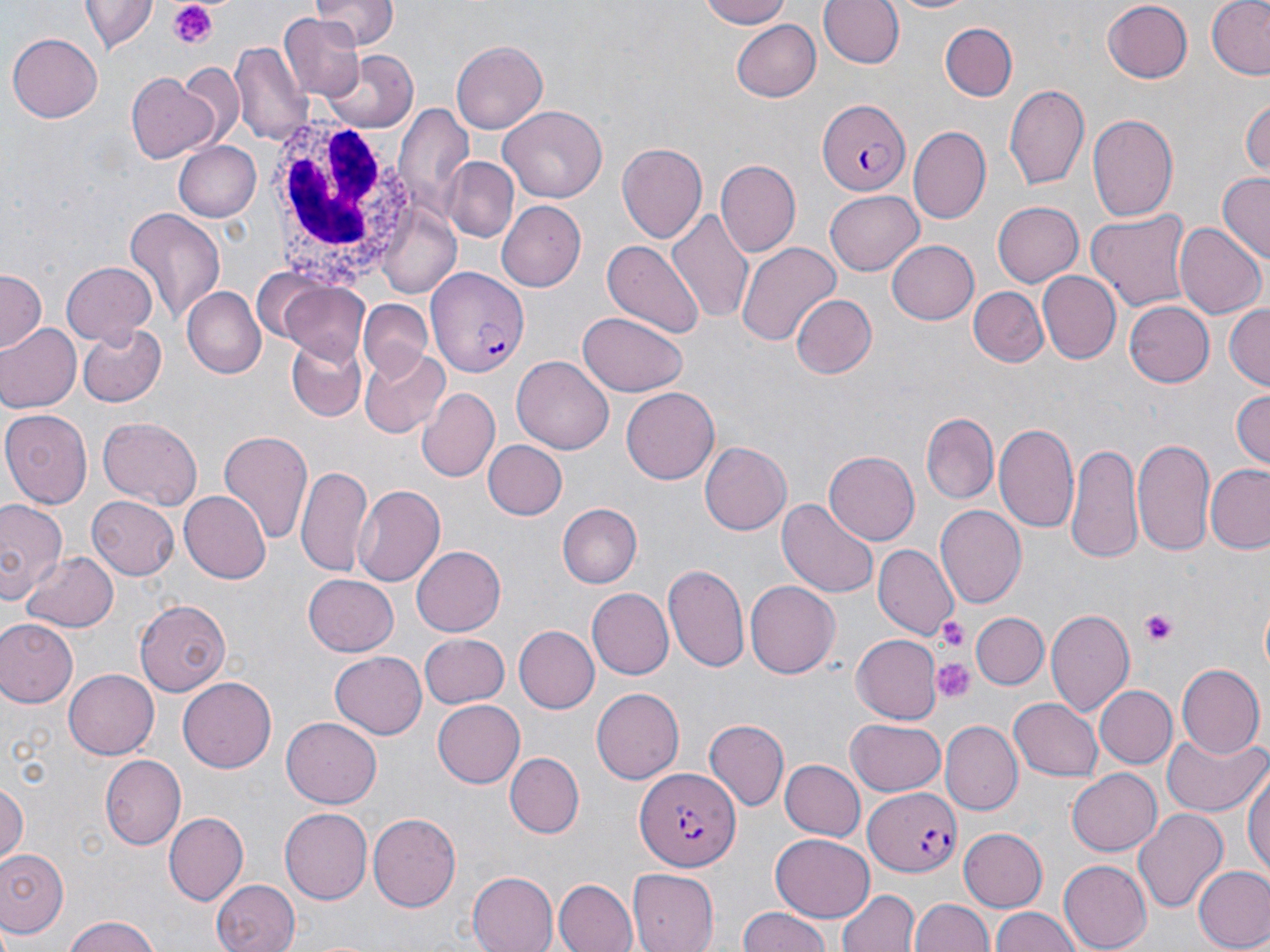 Approximate bounding boxes as named x1/y1/x2/y2 corners in pixels. White blood cell locations: (x1=257, y1=110, x2=423, y2=291). Uninfected red blood cell locations: (x1=313, y1=0, x2=396, y2=49), (x1=696, y1=0, x2=793, y2=29), (x1=819, y1=0, x2=905, y2=69), (x1=882, y1=0, x2=981, y2=16), (x1=1206, y1=0, x2=1270, y2=81), (x1=1101, y1=1, x2=1195, y2=84), (x1=82, y1=2, x2=156, y2=54), (x1=278, y1=15, x2=369, y2=101), (x1=732, y1=20, x2=821, y2=102), (x1=938, y1=20, x2=1017, y2=101), (x1=8, y1=29, x2=103, y2=120), (x1=450, y1=41, x2=546, y2=134), (x1=230, y1=42, x2=309, y2=146), (x1=324, y1=50, x2=417, y2=133), (x1=182, y1=63, x2=244, y2=145), (x1=126, y1=73, x2=220, y2=164), (x1=1005, y1=82, x2=1092, y2=191), (x1=1242, y1=97, x2=1269, y2=181), (x1=394, y1=103, x2=476, y2=220), (x1=499, y1=105, x2=609, y2=204), (x1=1088, y1=111, x2=1180, y2=226), (x1=909, y1=128, x2=990, y2=224), (x1=172, y1=139, x2=262, y2=221), (x1=615, y1=141, x2=708, y2=243), (x1=443, y1=157, x2=517, y2=239), (x1=716, y1=160, x2=800, y2=258), (x1=1217, y1=172, x2=1269, y2=265), (x1=824, y1=191, x2=924, y2=274), (x1=499, y1=200, x2=590, y2=292), (x1=993, y1=200, x2=1085, y2=287), (x1=378, y1=206, x2=461, y2=300), (x1=123, y1=208, x2=224, y2=322), (x1=668, y1=208, x2=755, y2=327), (x1=1087, y1=208, x2=1194, y2=312), (x1=1173, y1=222, x2=1265, y2=319), (x1=885, y1=240, x2=977, y2=324), (x1=602, y1=241, x2=704, y2=340), (x1=735, y1=243, x2=840, y2=350), (x1=60, y1=261, x2=157, y2=348), (x1=0, y1=271, x2=44, y2=356), (x1=1038, y1=271, x2=1121, y2=362), (x1=278, y1=281, x2=373, y2=365), (x1=184, y1=287, x2=265, y2=376), (x1=968, y1=288, x2=1049, y2=368), (x1=789, y1=293, x2=876, y2=379), (x1=1123, y1=300, x2=1215, y2=387), (x1=359, y1=301, x2=432, y2=377), (x1=1223, y1=302, x2=1270, y2=393), (x1=578, y1=313, x2=689, y2=396), (x1=75, y1=323, x2=165, y2=407), (x1=1, y1=324, x2=81, y2=412), (x1=283, y1=336, x2=368, y2=422), (x1=359, y1=346, x2=450, y2=436), (x1=514, y1=357, x2=614, y2=453), (x1=621, y1=386, x2=719, y2=485), (x1=1229, y1=387, x2=1270, y2=469), (x1=417, y1=388, x2=500, y2=485), (x1=1, y1=409, x2=92, y2=506), (x1=921, y1=414, x2=999, y2=504), (x1=97, y1=417, x2=203, y2=510), (x1=995, y1=421, x2=1079, y2=532), (x1=217, y1=429, x2=313, y2=550), (x1=1133, y1=438, x2=1214, y2=553), (x1=484, y1=440, x2=565, y2=519), (x1=1066, y1=441, x2=1143, y2=562), (x1=700, y1=442, x2=790, y2=535), (x1=825, y1=450, x2=921, y2=545), (x1=1205, y1=464, x2=1269, y2=554), (x1=295, y1=465, x2=371, y2=574), (x1=352, y1=484, x2=446, y2=586), (x1=180, y1=491, x2=272, y2=584), (x1=87, y1=496, x2=178, y2=580), (x1=0, y1=498, x2=68, y2=608), (x1=779, y1=498, x2=879, y2=599), (x1=558, y1=504, x2=642, y2=587), (x1=935, y1=505, x2=1027, y2=608), (x1=411, y1=544, x2=505, y2=637), (x1=874, y1=544, x2=959, y2=641), (x1=21, y1=552, x2=118, y2=632), (x1=662, y1=561, x2=752, y2=674), (x1=301, y1=574, x2=399, y2=657), (x1=743, y1=580, x2=839, y2=678), (x1=585, y1=589, x2=671, y2=680), (x1=135, y1=599, x2=229, y2=696), (x1=1045, y1=609, x2=1134, y2=717), (x1=971, y1=612, x2=1048, y2=690), (x1=0, y1=618, x2=79, y2=708), (x1=515, y1=626, x2=598, y2=711), (x1=420, y1=633, x2=511, y2=708), (x1=851, y1=635, x2=943, y2=724), (x1=329, y1=652, x2=426, y2=740), (x1=1175, y1=664, x2=1263, y2=759), (x1=64, y1=671, x2=158, y2=757), (x1=179, y1=677, x2=276, y2=773), (x1=1093, y1=684, x2=1176, y2=767), (x1=592, y1=687, x2=684, y2=785), (x1=1008, y1=697, x2=1103, y2=781), (x1=433, y1=700, x2=525, y2=786), (x1=283, y1=718, x2=382, y2=808), (x1=705, y1=718, x2=789, y2=811), (x1=845, y1=718, x2=946, y2=799), (x1=941, y1=721, x2=1022, y2=815), (x1=1161, y1=732, x2=1266, y2=816), (x1=506, y1=753, x2=584, y2=838), (x1=103, y1=755, x2=187, y2=848), (x1=1244, y1=758, x2=1270, y2=886), (x1=779, y1=759, x2=864, y2=841), (x1=1067, y1=769, x2=1161, y2=855), (x1=0, y1=781, x2=26, y2=866), (x1=1134, y1=807, x2=1228, y2=913), (x1=279, y1=808, x2=371, y2=904), (x1=164, y1=811, x2=248, y2=903), (x1=367, y1=812, x2=461, y2=911), (x1=959, y1=828, x2=1048, y2=910), (x1=771, y1=832, x2=876, y2=921), (x1=0, y1=848, x2=69, y2=939), (x1=1058, y1=860, x2=1150, y2=950), (x1=1193, y1=865, x2=1270, y2=951), (x1=627, y1=869, x2=718, y2=951), (x1=466, y1=872, x2=559, y2=952), (x1=209, y1=878, x2=299, y2=952), (x1=552, y1=878, x2=637, y2=952), (x1=837, y1=887, x2=918, y2=952), (x1=912, y1=898, x2=994, y2=952), (x1=992, y1=907, x2=1081, y2=952), (x1=736, y1=908, x2=837, y2=952), (x1=61, y1=915, x2=160, y2=952). Plasmodium falciparum-infected red blood cell locations: (x1=817, y1=99, x2=910, y2=194), (x1=426, y1=264, x2=531, y2=381), (x1=636, y1=770, x2=741, y2=875), (x1=865, y1=787, x2=961, y2=877). Platelet locations: (x1=168, y1=3, x2=220, y2=50), (x1=1139, y1=609, x2=1181, y2=645), (x1=935, y1=617, x2=970, y2=651), (x1=934, y1=657, x2=976, y2=705). Slide-level diagnosis: Plasmodium falciparum. May-Grünwald-Giemsa-stained preparation. Image is 1270×952 pixels. Thin blood smear. One field of a larger specimen. 1000x magnification. Optical microscopy.